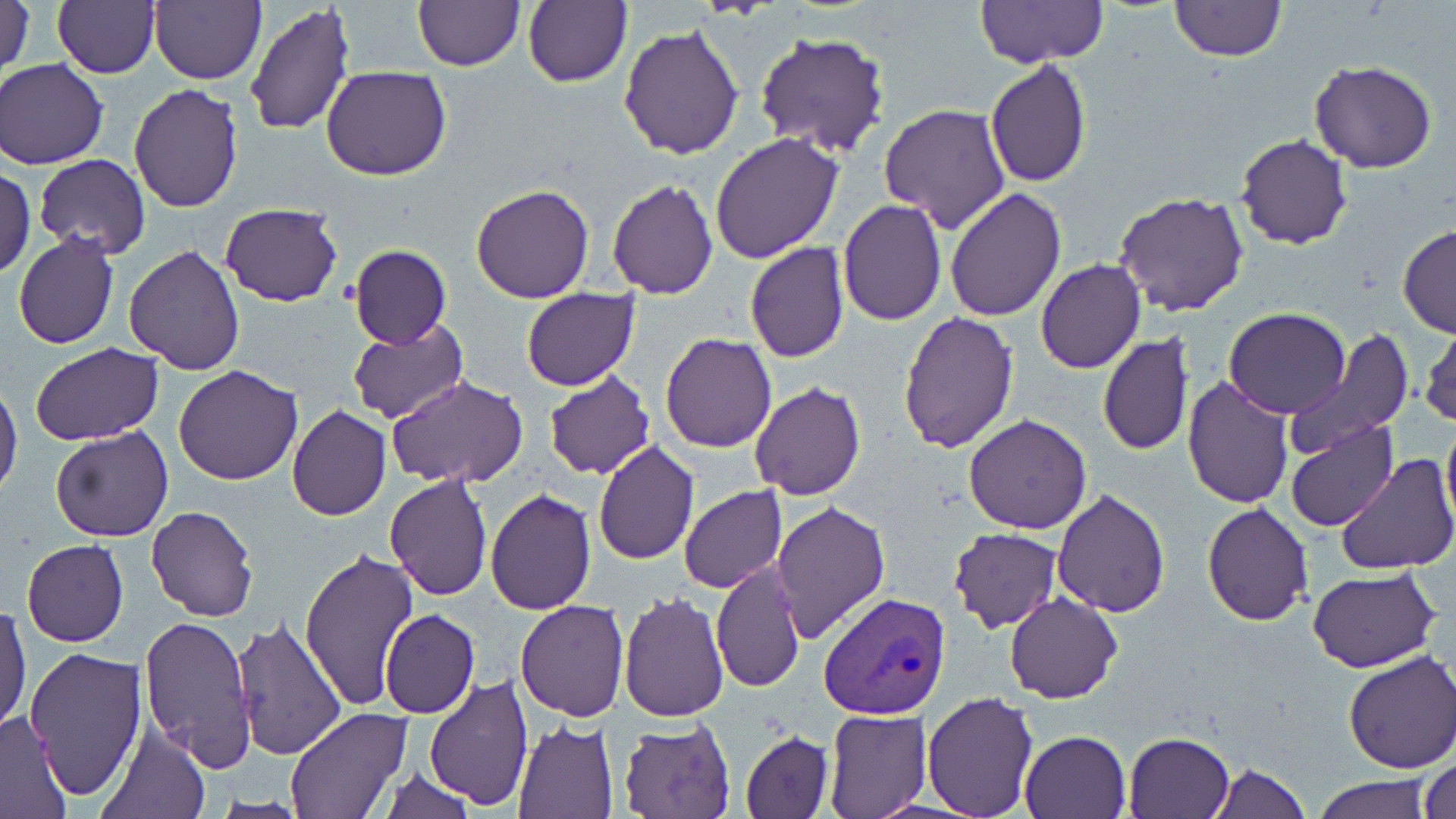
slide_level_diagnosis: Plasmodium vivax
uninfected_red_blood_cell_locations: 'approximate bounding boxes as [x1, y1, x2, y2] in pixels: [1, 0, 35, 78], [52, 0, 159, 78], [150, 0, 264, 84], [523, 0, 632, 88], [976, 1, 1108, 69], [1169, 1, 1286, 64], [412, 2, 523, 71], [245, 3, 354, 136], [619, 23, 747, 160], [755, 31, 890, 157], [1, 59, 108, 170], [984, 59, 1093, 188], [1309, 60, 1437, 173], [323, 65, 451, 181], [129, 82, 244, 213], [878, 102, 1010, 234], [710, 133, 842, 264], [1234, 134, 1352, 249], [34, 154, 151, 258], [0, 166, 35, 277], [607, 178, 718, 299], [471, 183, 594, 304], [945, 187, 1067, 321], [1114, 192, 1250, 317], [838, 200, 947, 325], [220, 202, 343, 307], [1396, 225, 1456, 338], [13, 234, 119, 350], [745, 242, 849, 363], [124, 244, 245, 376], [349, 245, 451, 348], [1036, 258, 1145, 375], [521, 287, 640, 392], [1225, 307, 1350, 419], [898, 311, 1019, 454], [348, 320, 468, 425], [1417, 323, 1456, 429], [1284, 329, 1413, 457], [660, 333, 778, 453], [1097, 333, 1194, 456], [31, 343, 163, 446], [174, 365, 303, 485], [543, 372, 656, 480], [1182, 375, 1295, 509], [386, 377, 530, 489], [0, 380, 23, 502], [749, 382, 867, 500], [287, 405, 390, 521], [1441, 408, 1456, 529], [964, 414, 1092, 534], [1285, 419, 1396, 531], [50, 424, 173, 542], [592, 442, 701, 566], [1335, 454, 1456, 574], [384, 473, 493, 600], [679, 486, 786, 594], [485, 488, 596, 613], [1052, 489, 1169, 618], [771, 499, 890, 642], [1202, 501, 1315, 625], [146, 506, 258, 621], [947, 527, 1062, 634], [21, 537, 128, 648], [300, 545, 418, 712], [712, 560, 805, 694], [1307, 567, 1439, 673], [619, 591, 728, 723], [1005, 592, 1121, 703], [515, 599, 629, 720], [0, 602, 31, 733], [380, 609, 479, 719], [139, 614, 255, 774], [229, 616, 347, 764], [24, 645, 148, 801], [1341, 650, 1454, 774], [424, 675, 533, 811], [922, 691, 1038, 818], [284, 708, 411, 818], [823, 708, 931, 818], [0, 710, 72, 817], [617, 719, 738, 819], [512, 722, 619, 818], [97, 723, 212, 819], [1020, 729, 1130, 818], [741, 731, 833, 819], [1122, 732, 1235, 818], [1417, 756, 1456, 819], [1208, 764, 1309, 819], [374, 766, 478, 819], [1312, 776, 1432, 819]'
preparation: thin blood smear
field_of_view: one of a larger specimen
modality: light microscopy
stain: May-Grünwald-Giemsa
magnification: 1000x
plasmodium_vivax_infected_red_blood_cell_locations: 'approximate bounding boxes as [x1, y1, x2, y2] in pixels: [821, 593, 950, 719]'
image_size: 1456×819 pixels